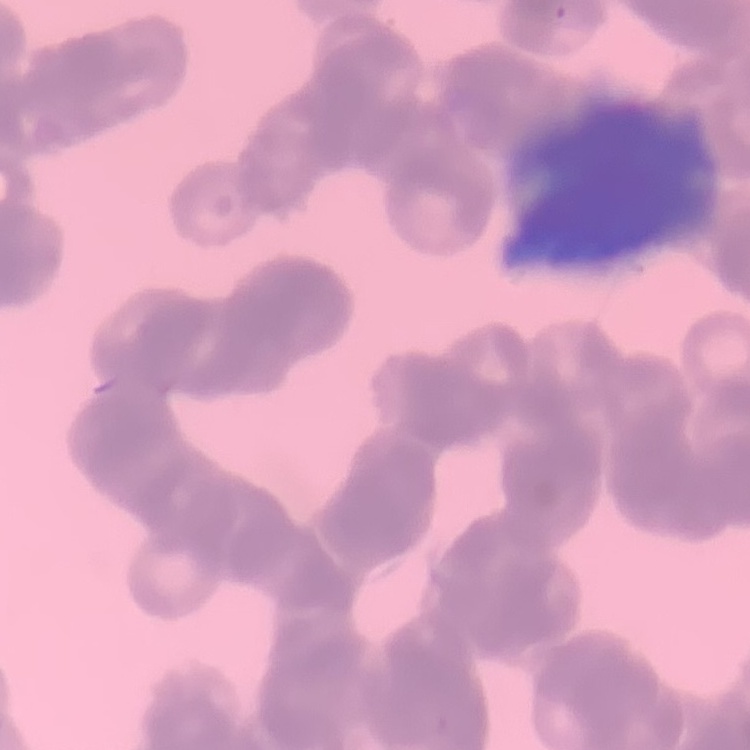

The erythrocytes exhibit rouleaux formation. Thin peripheral smear. Square crop of a larger photomicrograph. Stained with either Field's or Giemsa.